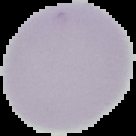 From a thin blood smear. Image is 136×136 pixels. Segmented cell region on a black background. Result: no malaria parasites detected.